State which cell type is depicted.
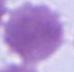

An erythrocyte.

magnification = 1000x
modality = micrograph